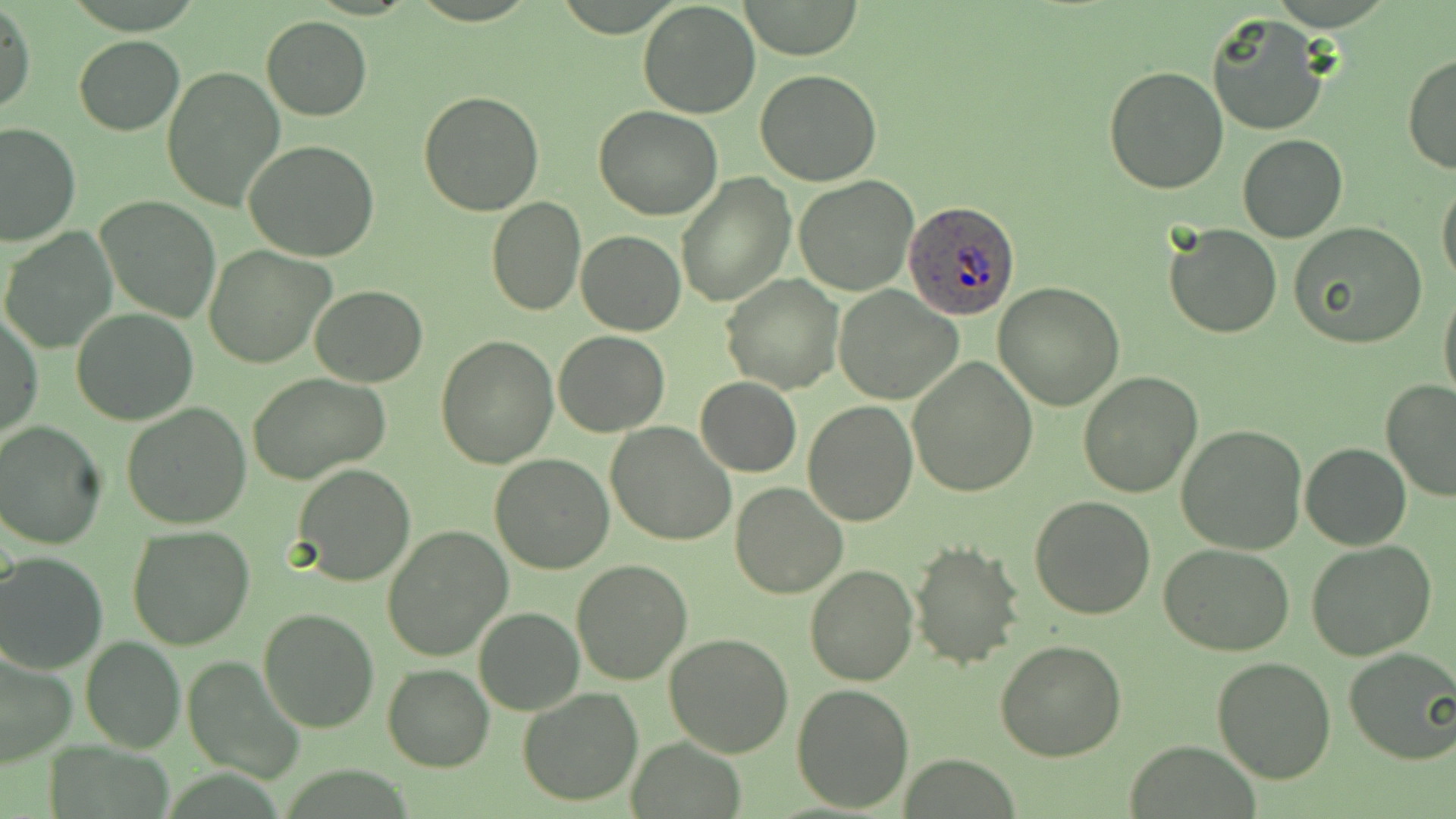
Approximate bounding boxes as [x1, y1, x2, y2] in pixels. Uninfected red blood cell locations: [638, 0, 762, 118], [738, 1, 864, 60], [0, 5, 35, 118], [1205, 13, 1330, 137], [261, 17, 372, 120], [74, 35, 184, 135], [1402, 52, 1456, 174], [162, 66, 287, 211], [1102, 66, 1228, 195], [756, 70, 884, 186], [419, 89, 546, 216], [594, 106, 724, 220], [0, 121, 79, 247], [1237, 135, 1348, 243], [245, 139, 381, 262], [676, 174, 794, 307], [794, 176, 921, 296], [1437, 179, 1456, 289], [484, 195, 587, 316], [96, 196, 220, 323], [1164, 222, 1283, 339], [1291, 223, 1429, 350], [1, 228, 117, 353], [576, 231, 685, 335], [204, 246, 336, 369], [721, 275, 843, 395], [993, 283, 1125, 410], [1438, 283, 1456, 413], [310, 285, 428, 386], [834, 287, 962, 404], [70, 308, 200, 425], [1, 310, 44, 443], [554, 330, 669, 436], [436, 335, 560, 468], [907, 357, 1038, 498], [247, 372, 392, 482], [1077, 372, 1202, 498], [695, 377, 801, 477], [1380, 378, 1456, 502], [802, 401, 918, 526], [119, 402, 251, 531], [0, 421, 106, 549], [605, 422, 736, 546], [1176, 425, 1308, 555], [1300, 442, 1411, 551], [489, 454, 615, 574], [292, 463, 416, 586], [731, 483, 849, 599], [1028, 495, 1156, 621], [127, 524, 256, 649], [382, 525, 514, 664], [910, 541, 1026, 669], [1307, 541, 1436, 659], [1161, 543, 1296, 657], [0, 551, 107, 671], [571, 558, 692, 685], [804, 564, 917, 686], [474, 606, 585, 714], [259, 607, 380, 733], [663, 633, 794, 758], [80, 635, 185, 753], [995, 639, 1127, 761], [1343, 647, 1456, 765], [0, 651, 74, 770], [181, 655, 306, 784], [1210, 656, 1337, 784], [383, 663, 495, 772], [792, 683, 914, 814], [517, 688, 643, 807], [627, 739, 746, 818], [1126, 740, 1260, 818]. Plasmodium ovale-infected red blood cell locations: [905, 200, 1022, 319]. Slide-level diagnosis: Plasmodium ovale. Thin blood film. May-Grünwald-Giemsa-stained preparation. Optical microscopy. Image is 1456×819 pixels. One field of a larger specimen. Captured at 1000x magnification.